Assess this cell for malaria.
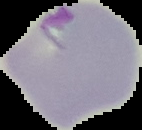
It is parasitized.

Image is 142×130 pixels. From a thin blood film. The area outside the segmented cell region is set to black.